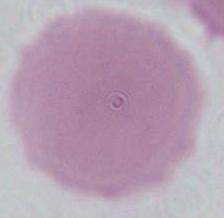
modality = micrograph
magnification = 1000x
identification = erythrocyte